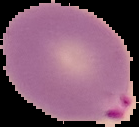
{
  "image_size": "139×127 pixels",
  "preparation": "thin blood smear",
  "result": "malaria parasites detected",
  "image_type": "cell region segmented out of the field of view; surrounding area masked to black"
}